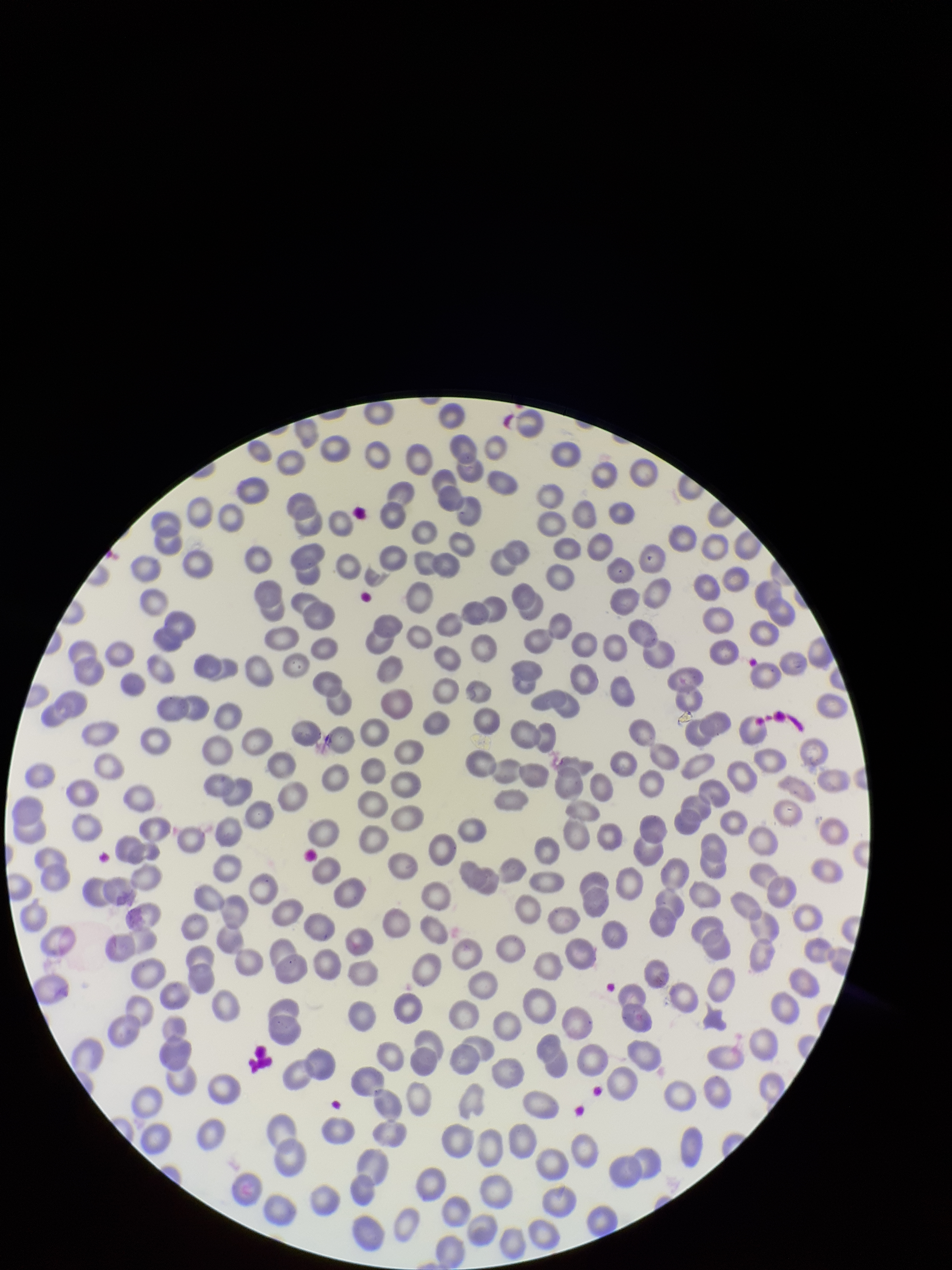
Smartphone photograph taken through the eyepiece of a microscope. Parasitized red blood cells: none seen. Parasitized red blood cell count: 0. Preparation: thin blood smear. Red blood cell count: 293. Single field of view. Patient malaria status: negative. Image is 952×1270 pixels. Stained with Giemsa.